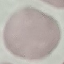
{
  "result": "no malaria parasites detected",
  "image_type": "cell patch, automatically extracted from a larger field of view and resized to 64 × 64 pixels",
  "stain": "Giemsa",
  "preparation": "thin blood smear",
  "capture": "smartphone camera at the microscope eyepiece"
}